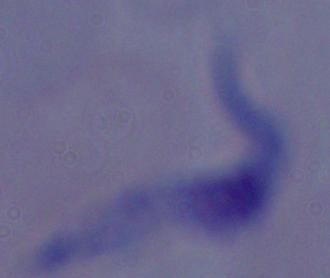

Summary:
  - Magnification: 1000x
  - Identification: trypanosome
  - Modality: photomicrograph